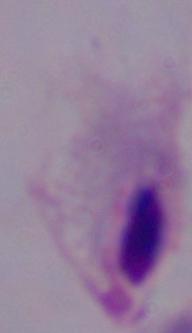

modality = micrograph
identification = trichomonad
magnification = 1000x